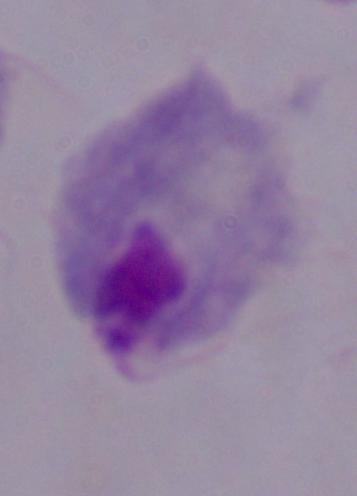 Photomicrograph. Captured at 1000x magnification. A trichomonad is seen.